Locate every blood parasite and identify its species.
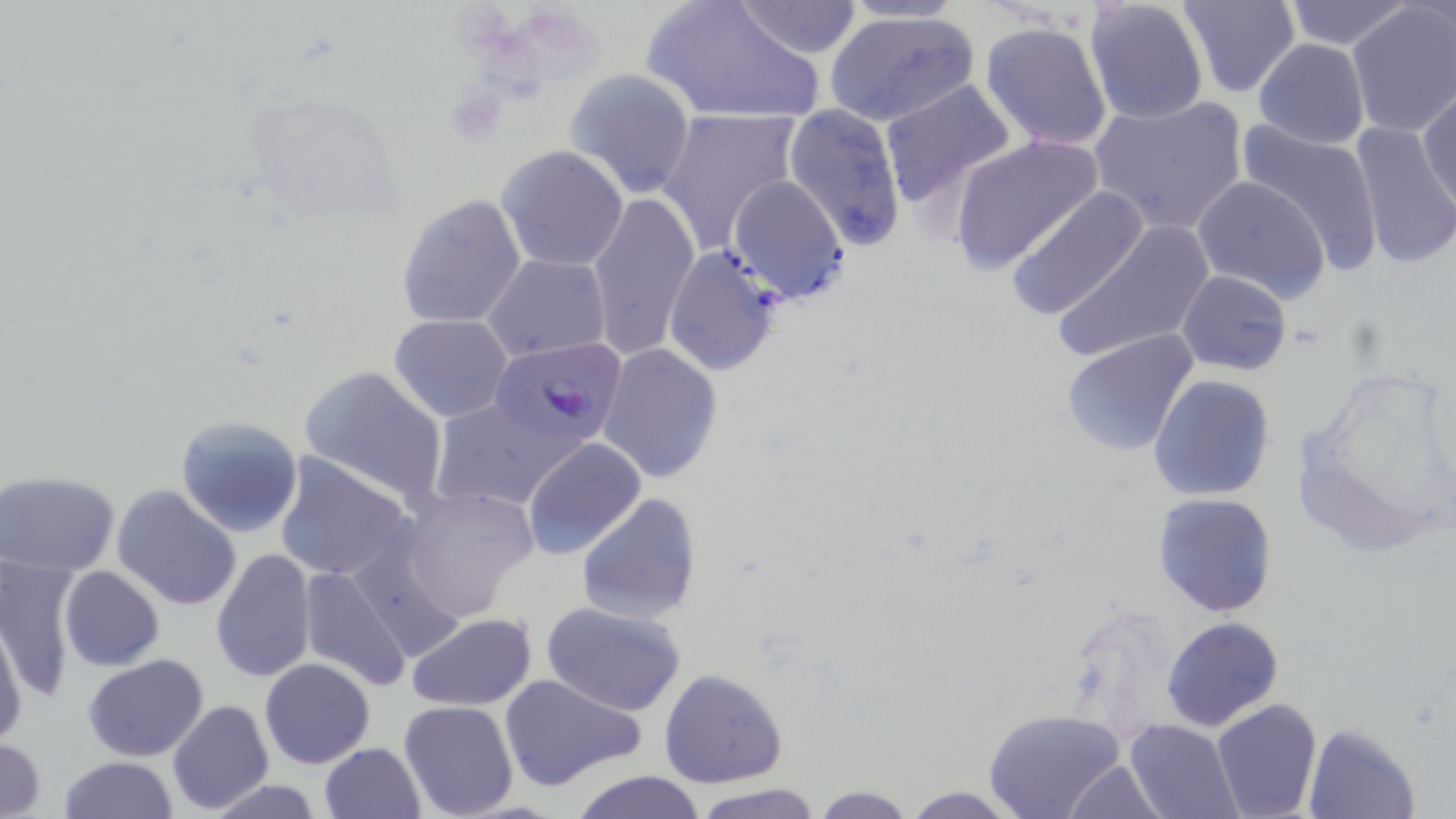

Approximate bounding boxes as [x1, y1, x2, y2] in pixels.
Plasmodium falciparum-infected red blood cells: [489, 338, 629, 447].
No Plasmodium ovale, Plasmodium malariae, Plasmodium vivax, Babesia divergens, or Trypanosoma brucei observed.

Platelet locations: [448, 84, 505, 144]. Uninfected red blood cell locations: [642, 0, 827, 125], [827, 0, 974, 26], [1176, 0, 1301, 100], [1280, 0, 1416, 50], [730, 1, 866, 59], [1083, 1, 1210, 125], [1345, 1, 1456, 140], [824, 8, 980, 126], [979, 21, 1113, 152], [1251, 39, 1370, 150], [563, 68, 695, 198], [878, 81, 1019, 212], [1418, 85, 1456, 212], [240, 91, 403, 230], [1089, 95, 1248, 234], [783, 103, 909, 251], [656, 105, 802, 255], [1349, 118, 1455, 271], [1235, 119, 1386, 268], [947, 134, 1105, 274], [497, 145, 629, 271], [728, 175, 851, 304], [1190, 176, 1330, 302], [1004, 185, 1150, 323], [588, 191, 700, 360], [396, 194, 528, 329], [1051, 219, 1212, 364], [657, 246, 784, 389], [484, 254, 610, 364], [1176, 270, 1293, 376], [389, 313, 512, 422], [1058, 328, 1199, 457], [597, 343, 723, 484], [1293, 364, 1451, 554], [298, 365, 449, 507], [1148, 376, 1276, 500], [428, 399, 577, 511], [174, 413, 305, 538], [520, 437, 647, 559], [273, 452, 414, 581], [1, 472, 121, 576], [395, 484, 541, 621], [112, 485, 242, 612], [576, 492, 701, 624], [1153, 492, 1276, 616], [210, 546, 316, 686], [0, 556, 79, 700], [298, 562, 414, 692], [59, 565, 164, 670], [539, 600, 688, 716], [405, 611, 538, 710], [1, 614, 26, 750], [1162, 616, 1285, 732], [82, 654, 209, 761], [258, 657, 375, 768], [658, 669, 787, 788], [498, 671, 649, 792], [166, 698, 274, 814], [1210, 698, 1323, 819], [397, 699, 519, 818], [983, 708, 1129, 819], [1123, 719, 1240, 819], [1302, 723, 1421, 819], [0, 737, 49, 819], [318, 742, 427, 819], [59, 756, 180, 818], [1059, 760, 1166, 817], [568, 769, 707, 819], [199, 779, 332, 818], [689, 781, 823, 819], [809, 784, 916, 817], [896, 786, 1028, 818]. Slide-level diagnosis: Plasmodium falciparum. May-Grünwald-Giemsa stain. 1000x magnification. Image is 1456×819 pixels. Thin blood film. Light microscopy. Single field of view.